Locate every Plasmodium parasite.
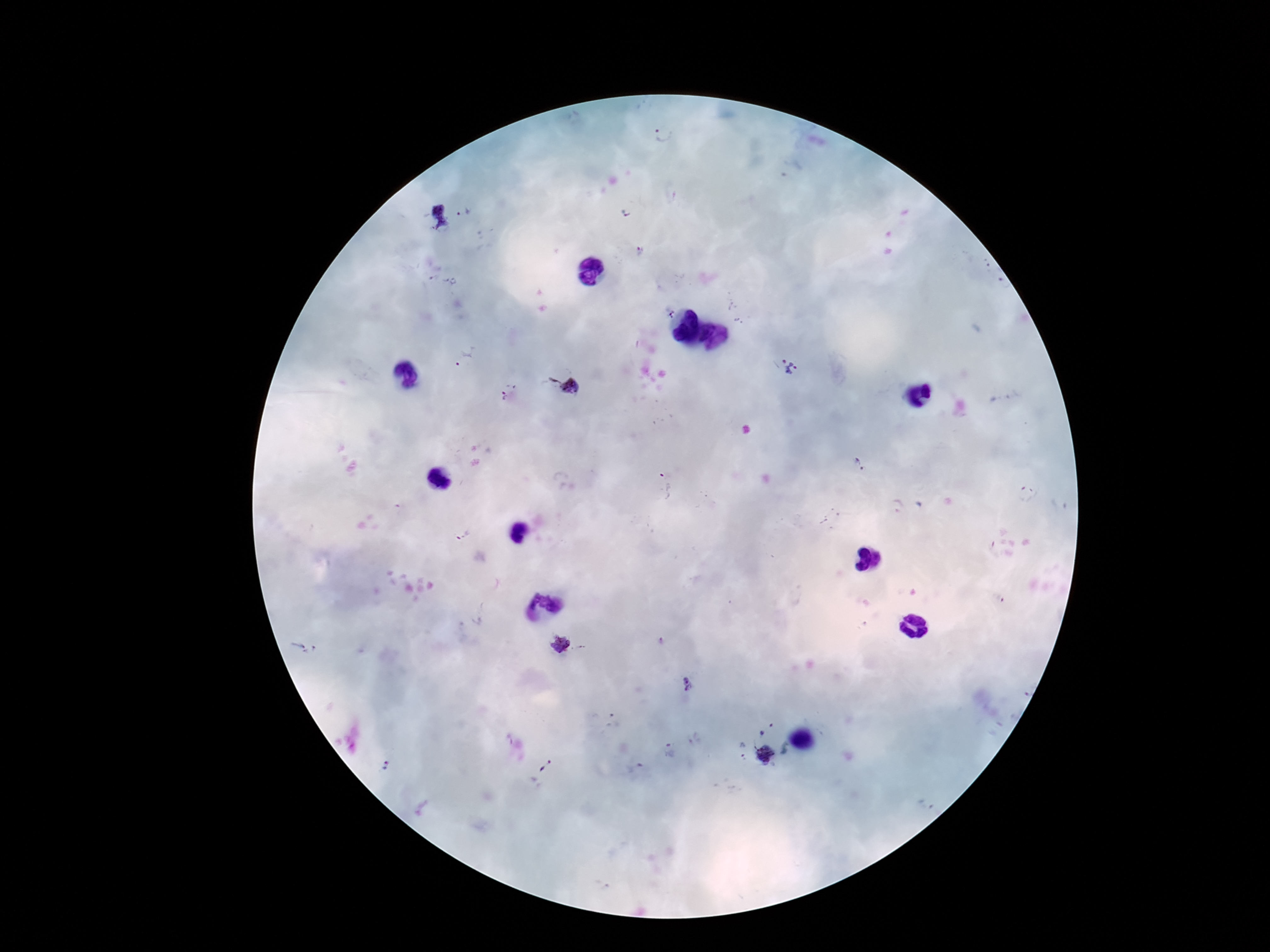

Approximate centers as {x, y} in pixels.
Plasmodium parasites: {662, 135}, {465, 212}, {626, 212}, {438, 217}, {640, 249}, {432, 278}, {445, 280}, {455, 282}, {670, 313}, {466, 356}, {788, 365}, {565, 387}, {508, 391}, {858, 466}, {665, 486}, {1026, 494}, {896, 504}, {463, 536}, {663, 640}, {561, 644}, {303, 647}, {689, 683}, {612, 721}, {761, 733}, {670, 751}, {742, 751}, {765, 754}, {384, 761}, {545, 765}, {634, 768}, {925, 805}.

Image is 1270×952 pixels. Patient malaria status: positive. Smartphone photograph taken through the microscope eyepiece. One field from this slide. Giemsa-stained preparation. 100x magnification. Thick peripheral-blood smear.